Locate every Plasmodium parasite.
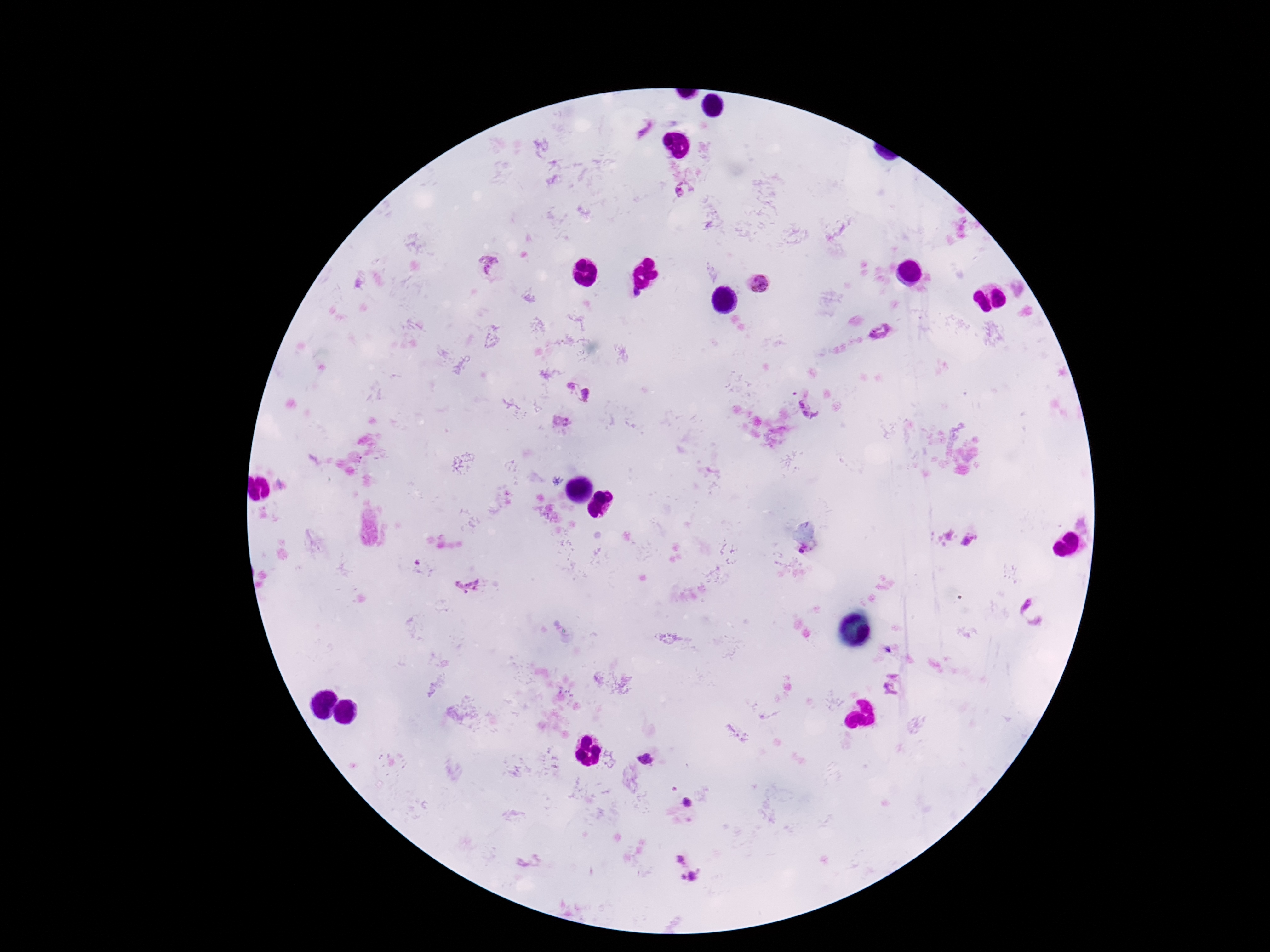

Approximate object centers, in pixels from the top-left corner.
Plasmodium parasites: (x=678, y=191), (x=489, y=253), (x=487, y=270), (x=758, y=284), (x=879, y=332), (x=571, y=385), (x=587, y=394), (x=811, y=408), (x=599, y=497), (x=609, y=498), (x=595, y=509), (x=605, y=512), (x=969, y=541), (x=803, y=550), (x=416, y=563), (x=467, y=583), (x=1034, y=611), (x=887, y=650), (x=892, y=673), (x=890, y=690), (x=646, y=759), (x=686, y=802), (x=681, y=858), (x=694, y=876), (x=683, y=877).

Summary:
  - Magnification: 100x
  - Preparation: thick blood smear
  - Patient malaria status: positive
  - Stain: Giemsa
  - Capture: smartphone camera through the microscope eyepiece
  - Image size: 1270×952 pixels
  - Field of view: single